Identify the blood parasite species.
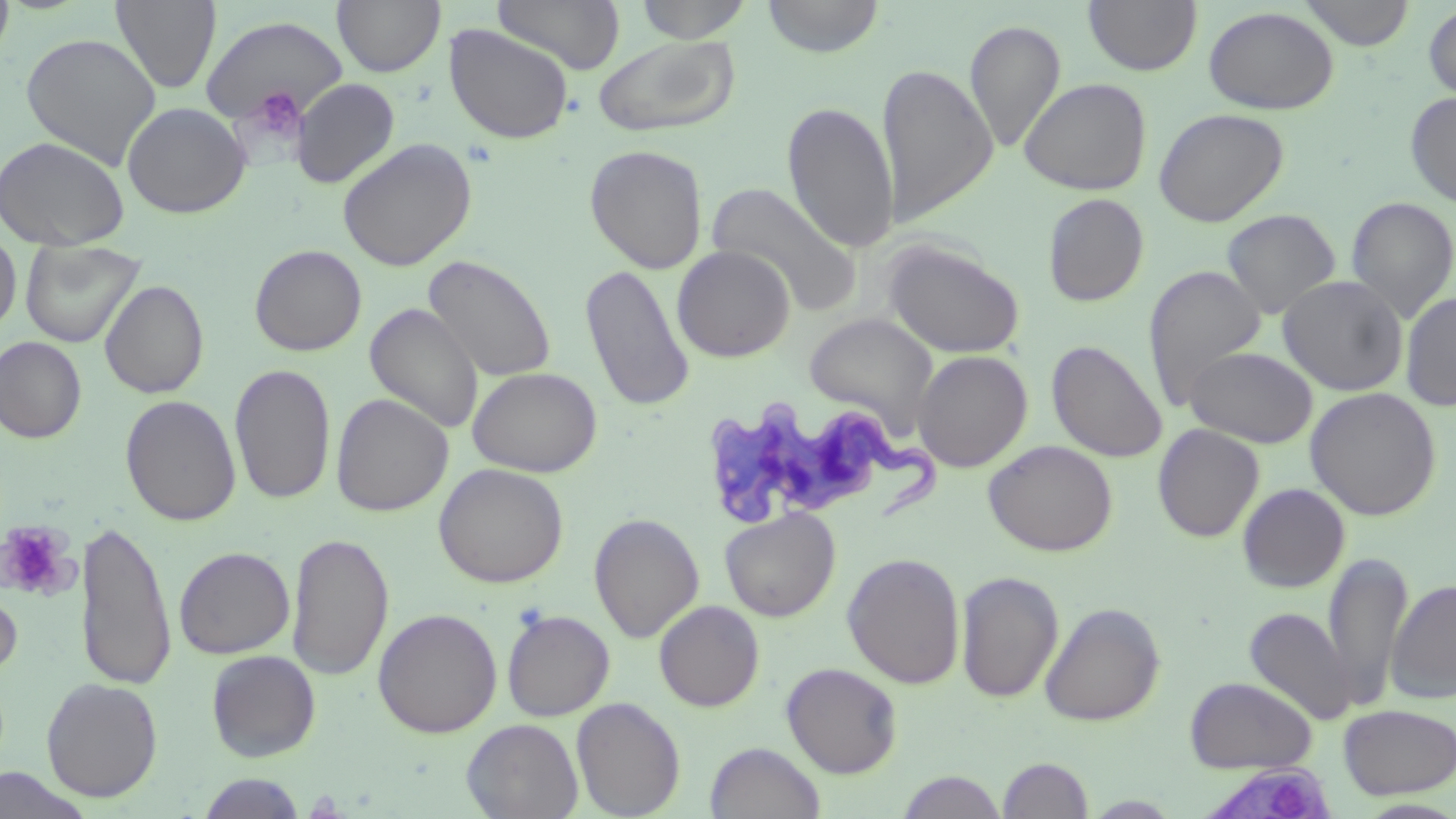
Trypanosoma brucei.

image_size: 1456×819 pixels
field_of_view: one of a larger specimen
stain: May-Grünwald-Giemsa
trypanosoma_brucei_locations: 'approximate bounding boxes as named x1/y1/x2/y2 corners in pixels: (x1=703, y1=400, x2=946, y2=528), (x1=1195, y1=764, x2=1335, y2=819)'
platelet_locations: 'approximate bounding boxes as named x1/y1/x2/y2 corners in pixels: (x1=245, y1=87, x2=307, y2=146), (x1=0, y1=520, x2=75, y2=598)'
uninfected_red_blood_cell_locations: 'approximate bounding boxes as named x1/y1/x2/y2 corners in pixels: (x1=0, y1=0, x2=15, y2=67), (x1=111, y1=0, x2=222, y2=94), (x1=332, y1=0, x2=445, y2=77), (x1=494, y1=0, x2=626, y2=75), (x1=634, y1=0, x2=754, y2=43), (x1=762, y1=0, x2=885, y2=58), (x1=1083, y1=0, x2=1203, y2=76), (x1=1299, y1=0, x2=1415, y2=50), (x1=1423, y1=2, x2=1456, y2=103), (x1=1203, y1=6, x2=1339, y2=115), (x1=200, y1=14, x2=347, y2=128), (x1=964, y1=20, x2=1066, y2=152), (x1=443, y1=23, x2=574, y2=144), (x1=20, y1=32, x2=161, y2=170), (x1=593, y1=35, x2=740, y2=138), (x1=879, y1=62, x2=998, y2=226), (x1=1019, y1=77, x2=1152, y2=196), (x1=291, y1=78, x2=400, y2=188), (x1=1405, y1=91, x2=1456, y2=209), (x1=782, y1=101, x2=899, y2=253), (x1=121, y1=102, x2=252, y2=218), (x1=1153, y1=108, x2=1289, y2=227), (x1=0, y1=135, x2=131, y2=252), (x1=337, y1=137, x2=477, y2=272), (x1=584, y1=144, x2=708, y2=274), (x1=707, y1=181, x2=860, y2=315), (x1=1042, y1=193, x2=1149, y2=307), (x1=1346, y1=196, x2=1456, y2=323), (x1=1222, y1=209, x2=1341, y2=320), (x1=0, y1=227, x2=21, y2=337), (x1=882, y1=238, x2=1024, y2=358), (x1=20, y1=239, x2=146, y2=348), (x1=249, y1=244, x2=367, y2=356), (x1=672, y1=245, x2=795, y2=362), (x1=424, y1=254, x2=557, y2=383), (x1=580, y1=263, x2=695, y2=413), (x1=1143, y1=265, x2=1266, y2=411), (x1=1277, y1=275, x2=1408, y2=396), (x1=99, y1=280, x2=209, y2=399), (x1=1400, y1=291, x2=1456, y2=412), (x1=365, y1=303, x2=484, y2=435), (x1=804, y1=312, x2=938, y2=434), (x1=0, y1=336, x2=87, y2=443), (x1=1047, y1=340, x2=1168, y2=463), (x1=1185, y1=345, x2=1318, y2=448), (x1=912, y1=350, x2=1033, y2=472), (x1=230, y1=363, x2=335, y2=506), (x1=468, y1=366, x2=602, y2=477), (x1=1305, y1=387, x2=1441, y2=520), (x1=330, y1=393, x2=453, y2=517), (x1=120, y1=395, x2=241, y2=526), (x1=1153, y1=424, x2=1264, y2=542), (x1=984, y1=439, x2=1118, y2=556), (x1=433, y1=463, x2=569, y2=588), (x1=1237, y1=483, x2=1350, y2=592), (x1=719, y1=507, x2=840, y2=621), (x1=589, y1=513, x2=705, y2=642), (x1=74, y1=518, x2=177, y2=692), (x1=286, y1=531, x2=393, y2=681), (x1=75, y1=532, x2=285, y2=680), (x1=174, y1=546, x2=295, y2=659), (x1=1323, y1=549, x2=1413, y2=711), (x1=843, y1=552, x2=965, y2=689), (x1=955, y1=570, x2=1064, y2=704), (x1=1386, y1=579, x2=1456, y2=704), (x1=0, y1=582, x2=22, y2=681), (x1=653, y1=600, x2=764, y2=711), (x1=1040, y1=602, x2=1165, y2=726), (x1=1244, y1=606, x2=1357, y2=726), (x1=372, y1=607, x2=503, y2=738), (x1=501, y1=609, x2=615, y2=721), (x1=206, y1=650, x2=321, y2=762), (x1=782, y1=662, x2=902, y2=777), (x1=1185, y1=676, x2=1316, y2=773), (x1=41, y1=677, x2=163, y2=802), (x1=572, y1=697, x2=685, y2=818), (x1=1338, y1=703, x2=1456, y2=799), (x1=462, y1=718, x2=583, y2=819), (x1=705, y1=742, x2=826, y2=818), (x1=997, y1=757, x2=1094, y2=818), (x1=0, y1=767, x2=92, y2=819), (x1=896, y1=770, x2=1006, y2=818), (x1=196, y1=773, x2=308, y2=818), (x1=1085, y1=795, x2=1182, y2=817)'
magnification: 1000x
preparation: thin blood film
modality: light microscopy